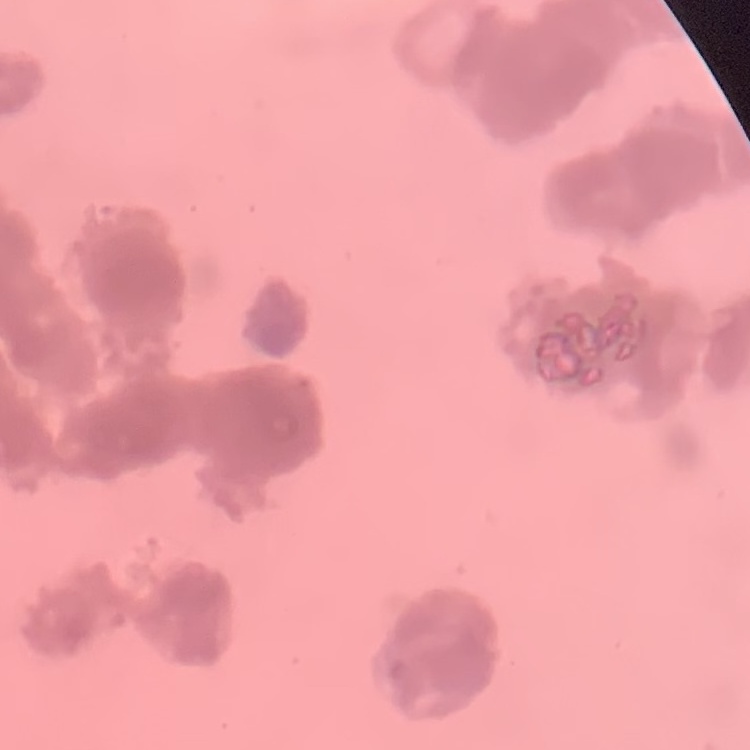

The erythrocytes exhibit rouleaux formation. Stained with either Field's or Giemsa. Square crop of a larger photomicrograph. Thin blood smear.